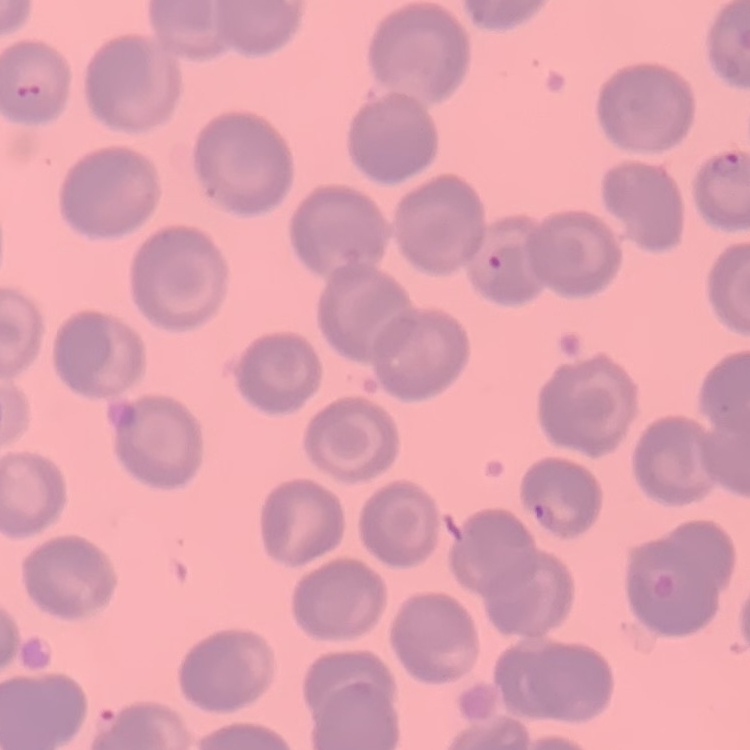

{
  "red_blood_cell_morphology": "no rouleaux formation",
  "image_type": "one tile cut from a larger photomicrograph",
  "stain": "Field's or Giemsa",
  "preparation": "thin blood smear"
}